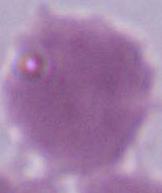

Photomicrograph. 1000x magnification. An erythrocyte is shown.